Identify the blood parasite species.
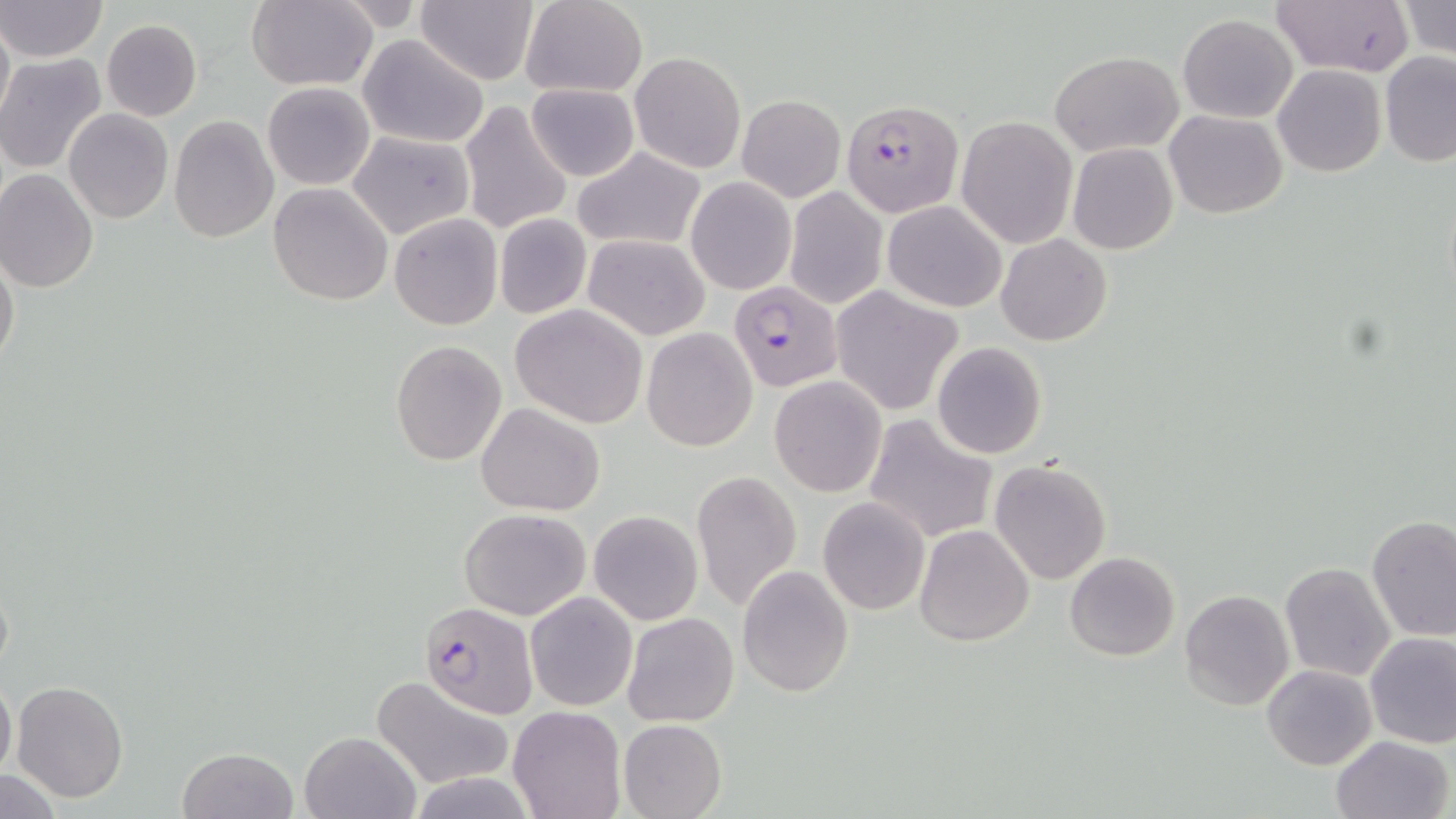

Plasmodium falciparum.

{
  "modality": "optical microscopy",
  "plasmodium_falciparum_infected_red_blood_cell_locations": "approximate bounding boxes as (x1, y1, x2, y2) in pixels: (842, 98, 963, 217), (728, 280, 842, 391), (421, 601, 540, 717)",
  "field_of_view": "single",
  "stain": "May-Grünwald-Giemsa",
  "uninfected_red_blood_cell_locations": "approximate bounding boxes as (x1, y1, x2, y2) in pixels: (1, 0, 108, 62), (416, 0, 541, 86), (1272, 0, 1415, 77), (245, 1, 377, 90), (520, 1, 649, 97), (1397, 1, 1456, 59), (0, 10, 13, 126), (1178, 13, 1298, 122), (101, 18, 203, 120), (357, 35, 490, 147), (629, 51, 746, 173), (1049, 51, 1183, 156), (1378, 52, 1456, 166), (0, 54, 106, 173), (1272, 64, 1386, 177), (262, 81, 376, 190), (525, 83, 640, 182), (737, 95, 845, 203), (458, 99, 573, 236), (63, 108, 173, 223), (1164, 110, 1288, 218), (955, 114, 1077, 249), (168, 115, 279, 243), (348, 129, 476, 241), (1067, 143, 1178, 255), (572, 147, 707, 251), (0, 170, 99, 294), (684, 175, 796, 294), (268, 182, 394, 305), (784, 186, 888, 310), (883, 200, 1006, 313), (389, 213, 502, 329), (493, 213, 593, 321), (996, 234, 1112, 347), (582, 235, 710, 341), (0, 252, 20, 372), (831, 289, 961, 414), (510, 304, 650, 428), (641, 327, 758, 450), (391, 341, 506, 465), (933, 342, 1048, 459), (769, 376, 887, 496), (476, 404, 605, 515), (861, 413, 998, 545), (989, 459, 1112, 585), (691, 469, 803, 613), (818, 497, 931, 616), (460, 508, 590, 619), (589, 510, 702, 624), (1367, 515, 1456, 641), (913, 525, 1035, 646), (1064, 551, 1180, 661), (1280, 563, 1394, 681), (737, 564, 854, 698), (1178, 588, 1294, 711), (524, 591, 637, 711), (623, 613, 739, 727), (1365, 631, 1456, 748), (1261, 664, 1378, 770), (0, 674, 16, 782), (370, 675, 515, 790), (11, 679, 128, 803), (508, 706, 626, 819), (618, 719, 726, 819), (299, 732, 420, 819), (1330, 735, 1455, 819), (177, 747, 300, 819), (0, 771, 65, 818)",
  "preparation": "thin blood smear",
  "magnification": "1000x",
  "image_size": "1456×819 pixels"
}